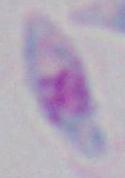

magnification = 1000x
identification = Toxoplasma gondii
modality = micrograph